Classify this cell by malaria status.
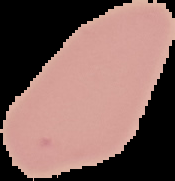
Uninfected.

preparation = thin blood smear
image size = 175×181 pixels
image type = cell region segmented out of the field of view; surrounding area masked to black